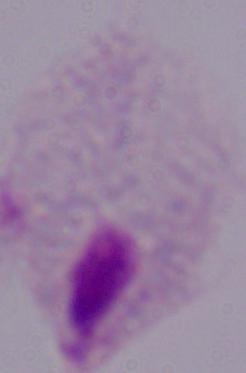

Micrograph. Captured at 1000x magnification. A trichomonad is shown.